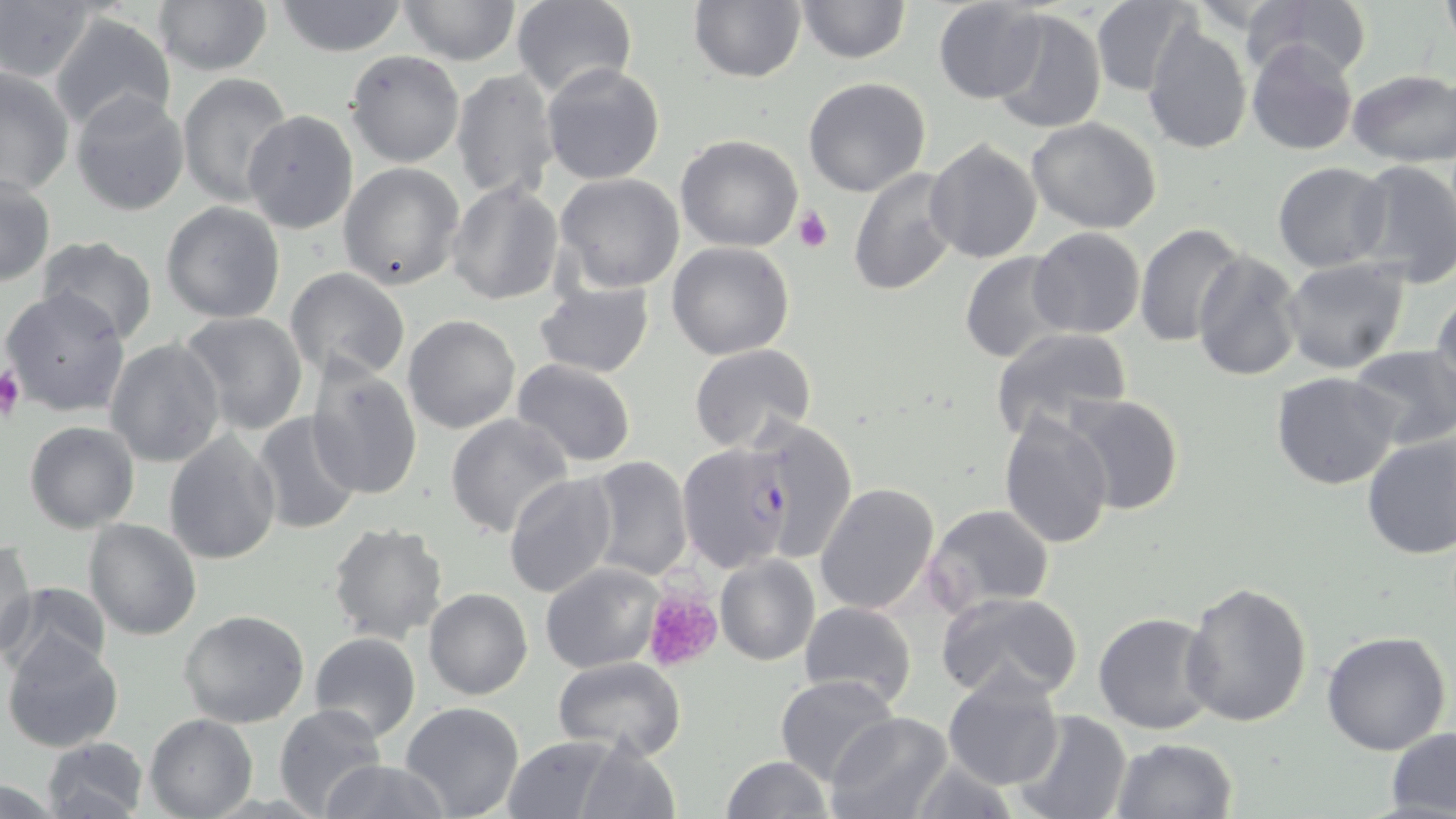
Approximate bounding boxes as [x1, y1, x2, y2] in pixels. Plasmodium falciparum-infected red blood cell locations: [677, 443, 794, 574]. Platelet locations: [794, 206, 834, 253], [0, 365, 26, 421], [643, 589, 725, 672]. Uninfected red blood cell locations: [151, 0, 273, 75], [510, 0, 638, 101], [688, 0, 807, 83], [795, 0, 910, 64], [932, 0, 1048, 104], [1239, 0, 1371, 79], [1438, 0, 1455, 45], [273, 1, 410, 56], [396, 1, 522, 64], [1089, 1, 1197, 95], [0, 2, 98, 83], [989, 8, 1107, 135], [48, 11, 176, 136], [1141, 22, 1252, 155], [1246, 39, 1359, 155], [346, 50, 466, 168], [540, 61, 668, 185], [1, 65, 74, 195], [450, 68, 561, 204], [1348, 70, 1455, 165], [177, 73, 294, 211], [803, 77, 931, 197], [70, 90, 190, 216], [241, 109, 359, 233], [1026, 117, 1162, 234], [675, 135, 805, 253], [924, 138, 1043, 263], [1349, 158, 1456, 290], [1273, 162, 1392, 273], [338, 163, 465, 291], [847, 167, 962, 298], [555, 172, 686, 294], [1, 174, 54, 286], [446, 181, 564, 306], [160, 201, 287, 323], [1136, 224, 1245, 349], [1028, 228, 1145, 339], [37, 236, 159, 345], [666, 241, 795, 360], [1191, 250, 1303, 380], [959, 252, 1075, 365], [1279, 257, 1410, 375], [284, 268, 412, 385], [533, 282, 654, 379], [1432, 287, 1456, 411], [3, 288, 130, 416], [178, 310, 308, 436], [403, 315, 521, 435], [989, 327, 1133, 443], [105, 337, 228, 468], [688, 342, 816, 452], [1347, 346, 1456, 451], [512, 358, 637, 469], [307, 363, 423, 501], [1270, 372, 1401, 491], [1064, 393, 1184, 516], [251, 411, 363, 534], [997, 411, 1114, 550], [446, 412, 575, 539], [745, 417, 858, 563], [23, 420, 139, 533], [164, 431, 281, 565], [1361, 431, 1456, 561], [585, 456, 692, 580], [502, 473, 618, 599], [814, 481, 942, 615], [922, 503, 1056, 616], [83, 519, 201, 640], [327, 522, 448, 644], [0, 540, 37, 661], [714, 554, 820, 666], [538, 562, 664, 671], [1181, 580, 1314, 728], [4, 581, 111, 680], [424, 587, 532, 699], [936, 591, 1085, 707], [799, 600, 916, 710], [179, 610, 311, 729], [1093, 611, 1218, 735], [1321, 630, 1452, 756], [310, 632, 421, 742], [3, 634, 125, 753], [553, 656, 688, 762], [941, 670, 1064, 791], [774, 674, 899, 787], [400, 701, 526, 819], [273, 704, 390, 817], [1013, 709, 1132, 819], [823, 712, 952, 819], [144, 714, 258, 819], [1385, 728, 1456, 816], [502, 734, 629, 816], [41, 736, 149, 817], [568, 736, 682, 818], [1111, 737, 1238, 819], [721, 756, 834, 818], [903, 758, 1019, 819], [319, 759, 448, 819], [0, 780, 66, 818]. Slide-level diagnosis: Plasmodium falciparum. Thin blood film. May-Grünwald-Giemsa stain. One field of a larger specimen. Captured at 1000x magnification. Image is 1456×819 pixels. Optical microscopy.